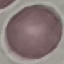

Summary:
  - Malaria status: uninfected
  - Preparation: thin smear
  - Stain: Giemsa
  - Image type: cell patch, automatically extracted from a larger field of view and resized to 64 × 64 pixels
  - Capture: smartphone camera at the microscope eyepiece